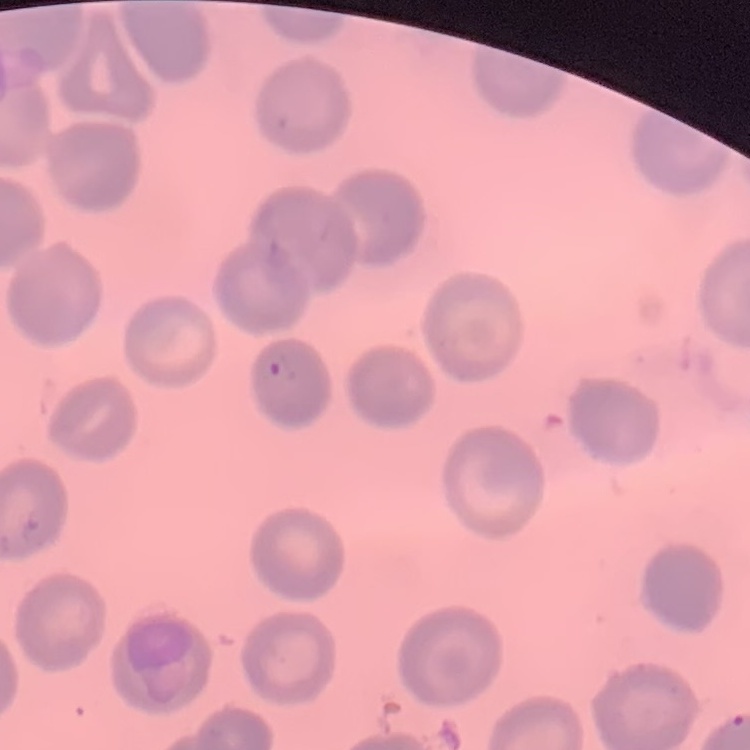

Summary:
  - Erythrocyte morphology: no rouleaux formation
  - Stain: Field's or Giemsa
  - Image type: one tile cut from a larger photomicrograph
  - Preparation: thin peripheral smear